Comment on the morphology of the red blood cells.
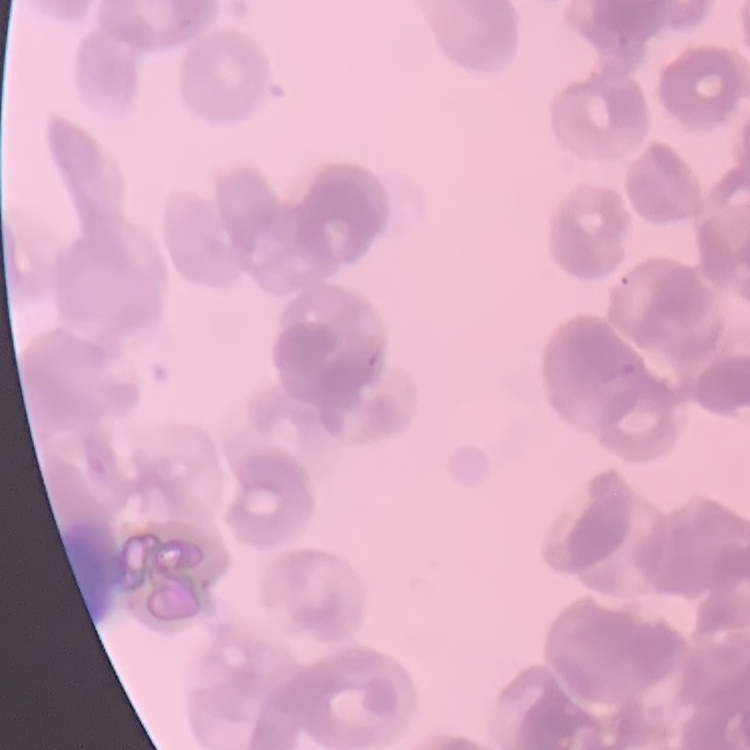

They show rouleaux formation.

Stained with either Field's or Giemsa. Square crop of a larger photomicrograph. Thin blood film.